Report the malaria status.
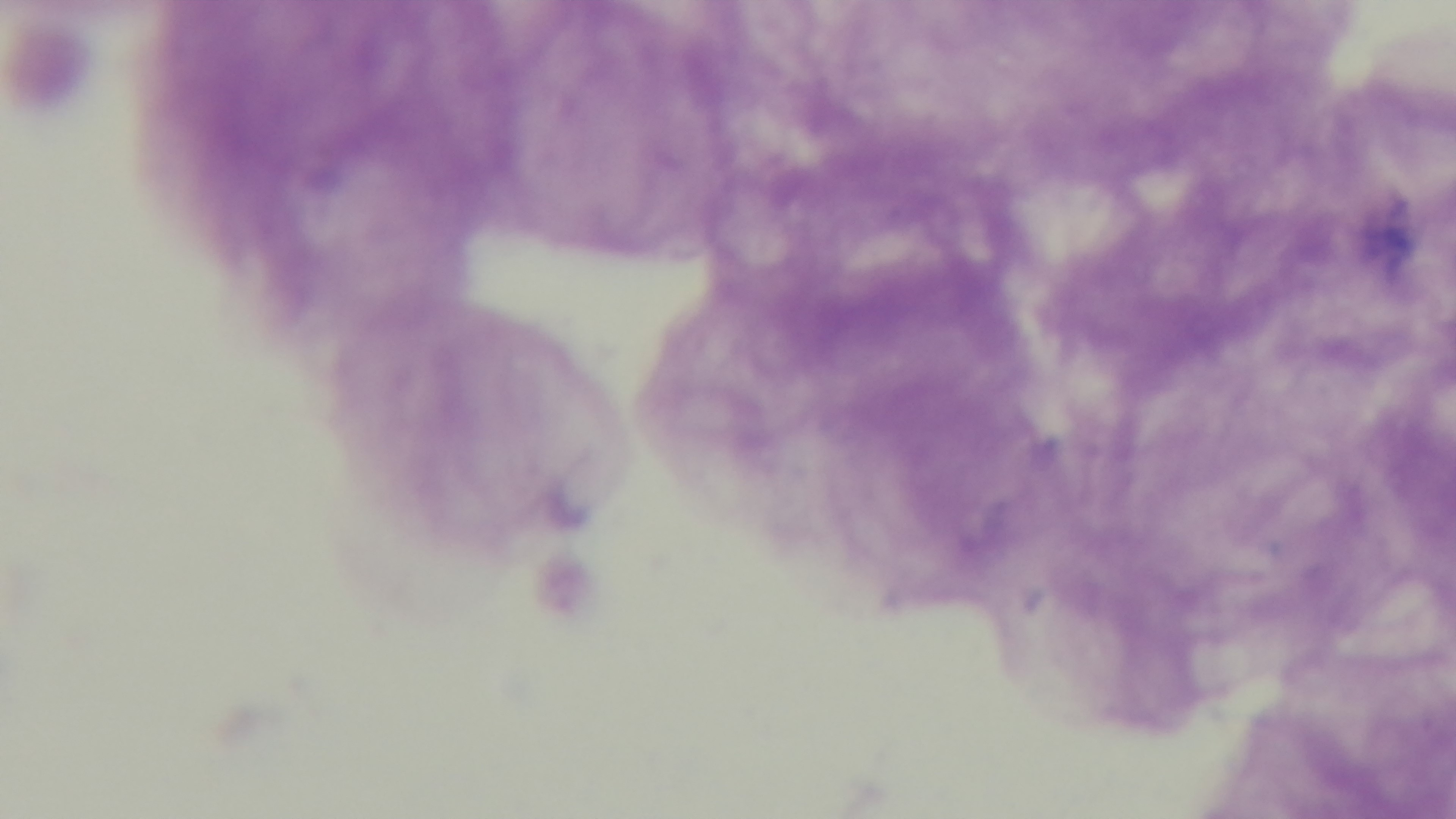
It is uninfected.

{
  "objective": "100x oil immersion",
  "preparation": "thick smear",
  "capture": "mounted 4K digital camera",
  "stain": "Giemsa",
  "field_of_view": "one from the slide",
  "modality": "light microscopy"
}